Name the parasite shown.
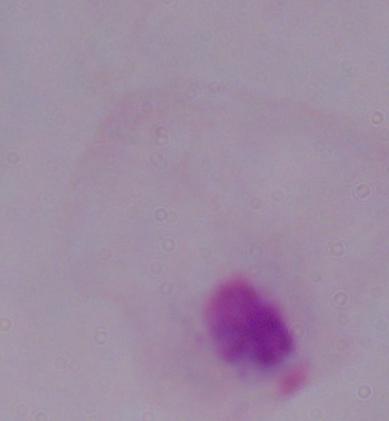
A trichomonad.

magnification = 1000x
modality = photomicrograph